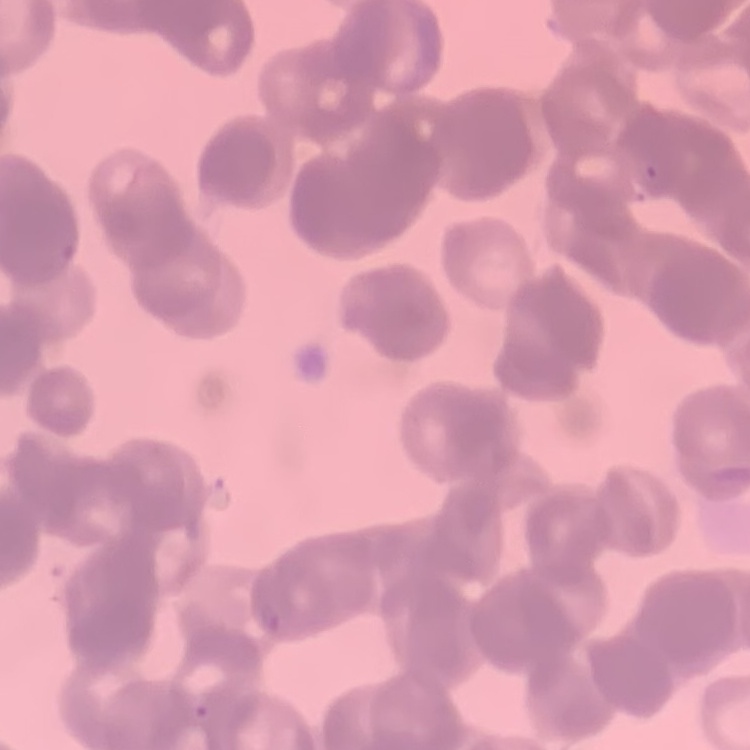

red_blood_cell_morphology: rouleaux formation
preparation: thin blood smear
stain: Field's or Giemsa
image_type: square crop of a larger photomicrograph